Classify this cell by malaria status.
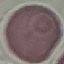
It is uninfected.

Summary:
  - Preparation: thin blood film
  - Stain: Giemsa
  - Image type: cell patch, automatically extracted from a larger field of view and resized to 64 × 64 pixels
  - Capture: smartphone camera at the microscope eyepiece